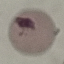
malaria status = uninfected
preparation = thin smear
capture = smartphone camera at the microscope eyepiece
image type = cell patch, automatically extracted from a larger field of view and resized to 64 × 64 pixels
stain = Giemsa